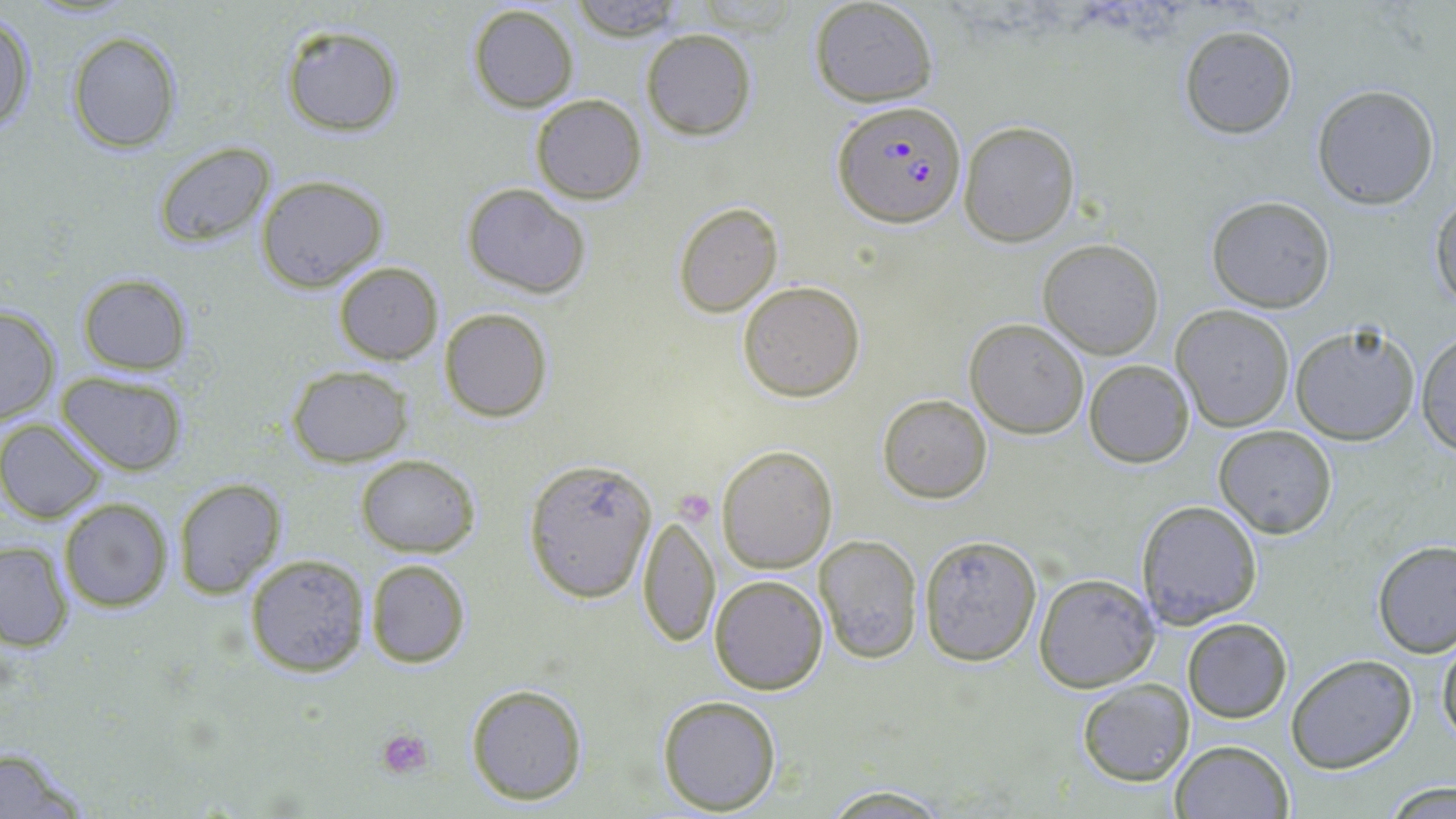

Approximate bounding boxes as (x1,y1)-(x2,y2) corner pairs in pixels. Uninfected red blood cell locations: (568,0)-(688,41), (810,0)-(939,107), (466,4)-(580,113), (0,13)-(36,134), (1178,24)-(1299,139), (280,25)-(405,135), (642,28)-(757,140), (68,29)-(182,154), (1311,84)-(1440,209), (530,94)-(647,204), (958,120)-(1081,248), (154,142)-(274,249), (255,174)-(389,292), (462,183)-(592,298), (1205,196)-(1336,313), (1429,197)-(1456,308), (673,202)-(783,317), (1037,237)-(1166,359), (333,261)-(443,365), (76,274)-(193,375), (738,279)-(867,402), (0,302)-(61,428), (1170,304)-(1296,432), (439,308)-(552,422), (964,318)-(1089,439), (1287,320)-(1420,447), (1414,331)-(1456,456), (1084,359)-(1194,467), (286,364)-(413,467), (56,370)-(189,476), (878,393)-(993,503), (2,419)-(107,523), (1213,425)-(1337,538), (717,444)-(837,573), (357,455)-(481,557), (523,456)-(659,602), (171,478)-(286,600), (59,497)-(175,612), (1135,499)-(1263,629), (637,509)-(720,651), (917,533)-(1042,666), (813,534)-(924,662), (0,539)-(73,652), (1372,540)-(1456,658), (244,553)-(370,677), (366,559)-(470,669), (1033,571)-(1161,693), (709,573)-(828,694), (1182,617)-(1293,724), (1437,631)-(1456,750), (1285,655)-(1417,773), (1075,678)-(1194,786), (464,682)-(589,805), (657,693)-(782,813), (1170,740)-(1294,819), (0,745)-(96,818), (1376,779)-(1456,816), (817,784)-(956,816). Platelet locations: (673,489)-(711,523), (376,726)-(436,779). Plasmodium falciparum-infected red blood cell locations: (833,100)-(966,228). Slide-level diagnosis: Plasmodium falciparum. Captured at 1000x magnification. Optical microscopy. May-Grünwald-Giemsa-stained preparation. Image is 1456×819 pixels. Single field of view. Thin blood smear.